Classify this cell by malaria status.
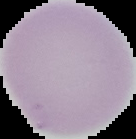

Uninfected.

preparation = thin blood film
image type = segmented cell region on a black background
image size = 136×139 pixels